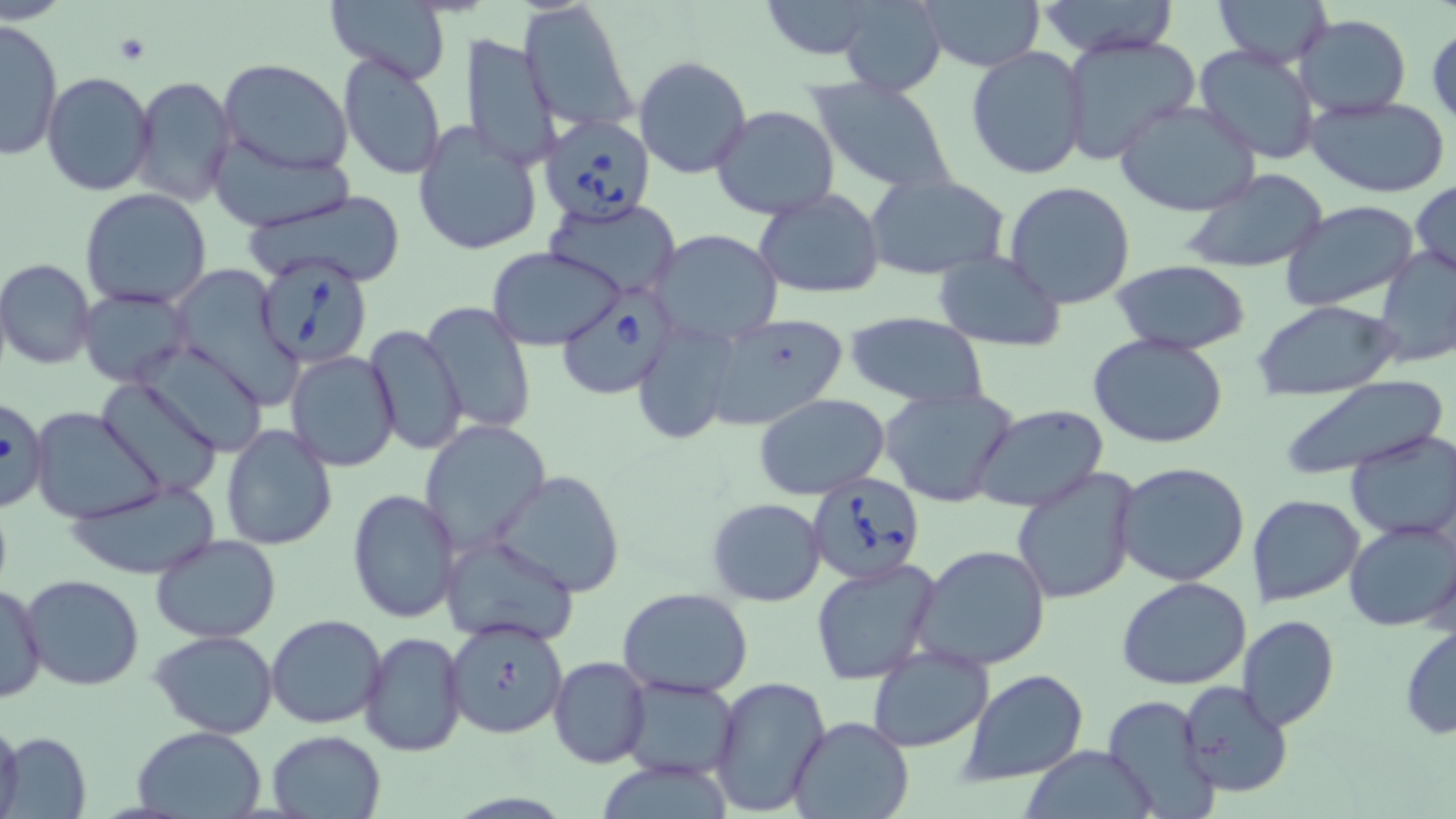

slide-level diagnosis = Babesia divergens
platelet locations = approximate bounding boxes as [x1, y1, x2, y2] in pixels: [112, 33, 151, 65]
uninfected red blood cell locations = approximate bounding boxes as [x1, y1, x2, y2] in pixels: [321, 0, 455, 86], [519, 0, 639, 133], [756, 0, 885, 61], [836, 0, 948, 98], [914, 0, 1044, 71], [1033, 0, 1185, 56], [1211, 0, 1332, 67], [1295, 15, 1411, 117], [0, 18, 62, 161], [1428, 25, 1456, 127], [462, 32, 564, 174], [1058, 34, 1202, 163], [1192, 43, 1322, 165], [965, 46, 1089, 181], [338, 55, 447, 179], [632, 55, 752, 180], [217, 59, 354, 176], [41, 71, 157, 194], [130, 75, 237, 209], [807, 77, 959, 193], [1303, 94, 1452, 199], [1114, 100, 1262, 217], [711, 106, 840, 221], [413, 122, 545, 256], [208, 141, 350, 233], [1179, 169, 1330, 275], [863, 173, 1011, 278], [1004, 181, 1136, 309], [1410, 181, 1456, 282], [80, 189, 213, 311], [241, 189, 408, 287], [755, 189, 886, 302], [541, 196, 682, 297], [1280, 200, 1421, 312], [650, 229, 783, 344], [488, 246, 627, 349], [1376, 247, 1456, 370], [934, 249, 1066, 351], [0, 259, 96, 370], [1111, 260, 1252, 355], [165, 263, 300, 408], [78, 287, 195, 386], [1254, 300, 1398, 400], [422, 302, 536, 434], [844, 309, 989, 410], [697, 314, 849, 432], [630, 320, 747, 446], [365, 324, 468, 456], [1087, 333, 1230, 450], [135, 341, 270, 457], [285, 351, 400, 471], [1278, 374, 1449, 480], [97, 378, 225, 497], [878, 386, 1017, 508], [754, 394, 890, 499], [0, 400, 54, 514], [971, 404, 1110, 514], [29, 407, 165, 525], [419, 419, 551, 555], [220, 424, 337, 551], [1345, 432, 1456, 542], [1113, 461, 1250, 587], [1011, 468, 1141, 605], [492, 470, 625, 596], [64, 478, 223, 581], [347, 489, 462, 624], [1246, 493, 1365, 607], [706, 498, 827, 606], [1344, 517, 1455, 631], [438, 531, 581, 647], [149, 533, 280, 642], [911, 544, 1053, 672], [810, 558, 940, 685], [21, 575, 147, 692], [1118, 576, 1253, 691], [1, 580, 47, 704], [618, 587, 754, 697], [265, 614, 387, 730], [1237, 615, 1339, 732], [443, 618, 569, 739], [1398, 622, 1455, 742], [148, 630, 280, 739], [359, 632, 467, 756], [866, 646, 995, 753], [549, 657, 652, 769], [960, 670, 1091, 784], [619, 675, 741, 781], [709, 676, 832, 817], [1176, 680, 1294, 800], [1101, 694, 1218, 818], [0, 715, 23, 819], [788, 715, 911, 819], [132, 726, 266, 818], [267, 730, 386, 818], [3, 732, 94, 817], [1018, 745, 1159, 818], [591, 759, 739, 817]
stain = May-Grünwald-Giemsa
Babesia divergens-infected red blood cell locations = approximate bounding boxes as [x1, y1, x2, y2] in pixels: [538, 114, 656, 226], [253, 254, 375, 372], [561, 284, 673, 401], [805, 473, 927, 585]
modality = light microscopy
image size = 1456×819 pixels
field of view = single
preparation = thin blood film
magnification = 1000x